Report the malaria status of this cell.
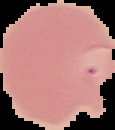
Parasitized.

Summary:
  - Image type: segmented cell region on a black background
  - Image size: 115×130 pixels
  - Preparation: thin blood smear